Locate malaria parasites and leukocytes.
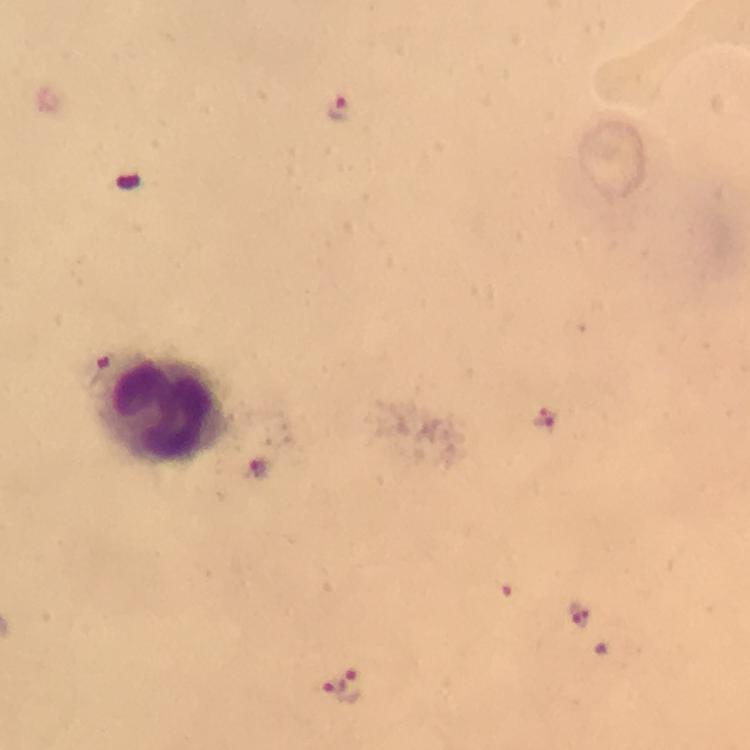

Approximate centers as [x, y] in pixels.
Malaria parasites: [337, 109], [102, 369], [547, 420], [256, 468], [505, 580], [582, 615], [606, 639], [333, 686], [353, 687].
Leukocytes: [160, 409].

100x magnification. Image is 750×750 pixels. Giemsa stain. Cropped region of a single field of view. Thick blood film. From a diagnostic examination for malaria. Smartphone photograph taken through a microscope. Immersion oil was used.